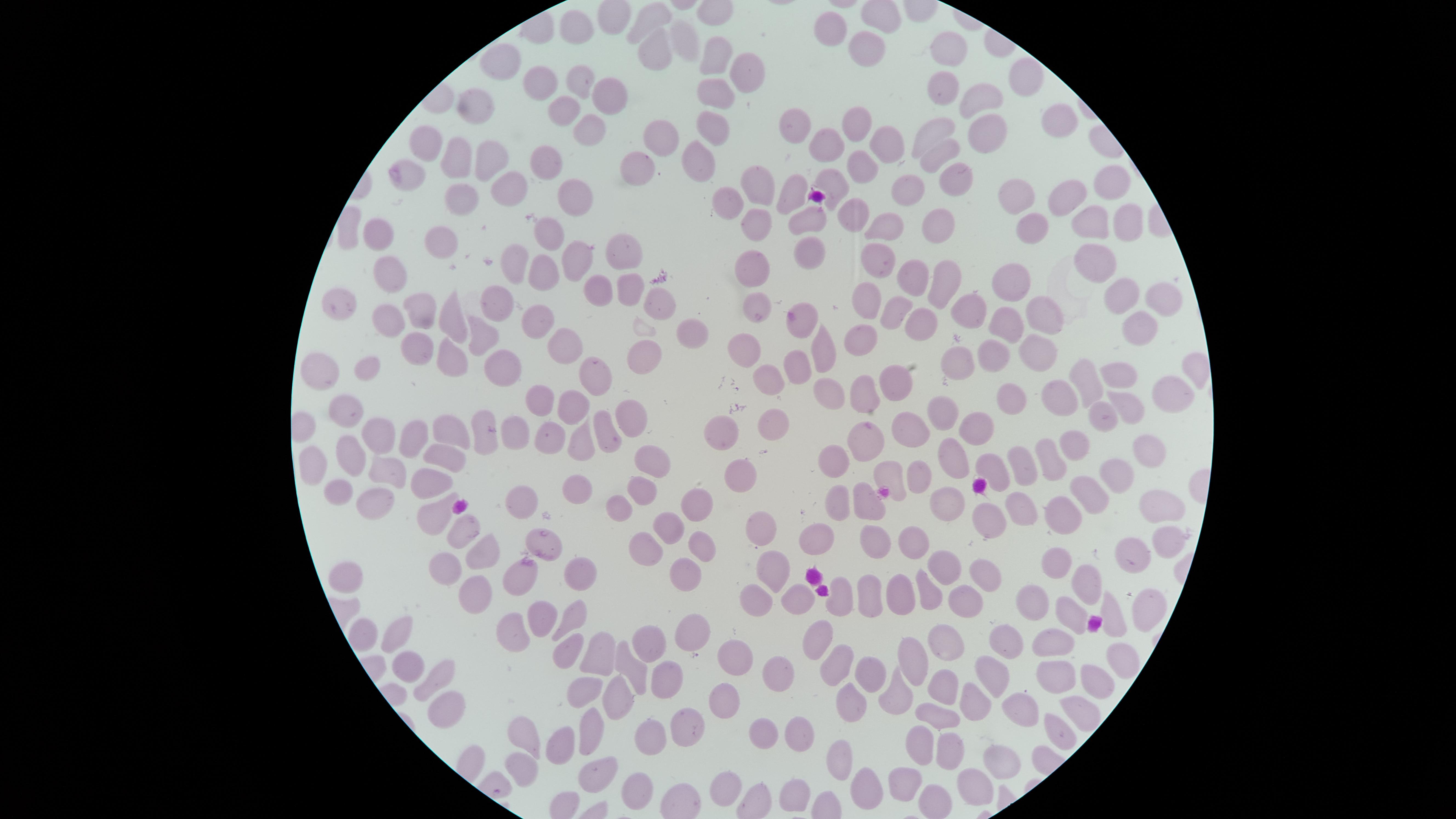

Approximate marker points as [x, y] in pixels.
Summary:
  - Uninfected red blood cells: [652, 18], [833, 27], [573, 30], [685, 38], [955, 46], [867, 49], [653, 50], [712, 58], [507, 63], [749, 67], [1021, 78], [576, 79], [545, 82], [939, 87], [710, 88], [602, 94], [477, 98], [981, 102], [566, 105], [586, 120], [709, 121], [1057, 124], [852, 130], [940, 130], [428, 131], [792, 131], [983, 132], [661, 137], [883, 137], [823, 145], [695, 151], [936, 153], [457, 158], [546, 158], [484, 161], [863, 167], [638, 174], [409, 176], [963, 181], [836, 184], [917, 185], [1107, 185], [515, 189], [755, 190], [571, 195], [1069, 195], [789, 196], [460, 197], [1012, 198], [733, 202], [812, 215], [853, 216], [941, 216], [1092, 220], [763, 221], [886, 224], [1132, 225], [1033, 229], [546, 234], [381, 236], [442, 236], [628, 249], [809, 252], [574, 258], [883, 262], [510, 265], [1099, 265], [752, 268], [389, 273], [541, 273], [914, 277], [943, 278], [597, 282], [1008, 283], [629, 288], [1124, 288], [1162, 295], [340, 300], [867, 301], [502, 303], [421, 305], [964, 307], [759, 309], [655, 311], [897, 314], [1042, 314], [385, 316], [455, 320], [536, 322], [796, 324], [1003, 324], [922, 325], [1137, 326], [860, 334], [685, 337], [482, 342], [740, 345], [412, 347], [1033, 349], [564, 350], [821, 350], [998, 353], [955, 355], [643, 356], [450, 358], [325, 361], [1192, 368], [367, 370], [502, 370], [1118, 371], [798, 372], [904, 373], [765, 378], [602, 379], [1087, 382], [825, 389], [866, 389], [1062, 389], [1170, 395], [1008, 397], [539, 401], [579, 404], [1131, 404], [336, 408], [943, 409], [628, 412], [1102, 412], [770, 423], [716, 426], [902, 426], [484, 429], [453, 430], [544, 430], [609, 431], [979, 431], [509, 433], [385, 434], [413, 434], [579, 441], [869, 444], [1082, 446], [355, 450], [445, 450], [954, 452], [1056, 452], [650, 455], [1145, 456], [839, 462], [1032, 465], [312, 466], [991, 466], [898, 471], [735, 472], [384, 473], [1121, 476], [431, 478], [922, 479], [574, 482], [643, 491], [336, 493], [1094, 493], [375, 498], [523, 498], [836, 502], [951, 502], [696, 504], [870, 504], [616, 505], [1155, 506], [1019, 507], [433, 510], [1064, 513], [984, 519], [753, 523], [666, 527], [458, 531], [1165, 536], [812, 537], [878, 540], [542, 541], [918, 543], [478, 546], [644, 551], [700, 551], [1131, 553], [771, 561], [1055, 562], [456, 570], [580, 570], [942, 570], [985, 571], [518, 580], [683, 582], [1088, 582], [354, 583], [921, 593], [874, 594], [1029, 594], [754, 595], [842, 595], [472, 597], [898, 597], [791, 598], [962, 600], [1137, 608], [1111, 611], [571, 614], [541, 617], [1070, 617], [514, 631], [687, 631], [821, 632], [364, 634], [1017, 637], [394, 638], [947, 640], [1050, 641], [643, 642], [566, 653], [595, 653], [730, 658], [1117, 658], [840, 660], [915, 661], [407, 668], [626, 670], [770, 671], [871, 671], [995, 674], [1056, 674], [664, 675], [1087, 681], [433, 684], [582, 688], [944, 692], [899, 693], [973, 697], [617, 701], [720, 701], [852, 703], [1081, 705], [443, 706], [1019, 706], [937, 717], [689, 729], [588, 730], [1053, 730], [758, 735], [795, 735], [920, 741], [526, 742], [648, 742], [554, 745], [943, 748], [835, 758], [998, 760], [519, 766], [590, 767], [905, 776], [723, 781], [790, 785], [634, 786], [859, 790], [972, 790], [930, 794]
  - Field of view: single
  - Stain: Giemsa
  - Image size: 1456×819 pixels
  - Preparation: thin blood smear
  - Visible region: circular
  - Capture: smartphone photograph through the microscope eyepiece
  - Presence: no malaria parasites detected